State which parasite is depicted.
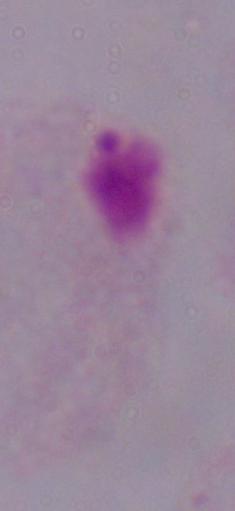
A trichomonad.

Summary:
  - Modality: photomicrograph
  - Magnification: 1000x